Report the malaria status of this cell.
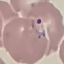
Parasitized.

Thin blood smear. Cell patch, automatically extracted from a larger field of view and resized to 64 × 64 pixels. Giemsa-stained preparation. Acquired by smartphone through the microscope eyepiece.